Describe the morphology of the red blood cells.
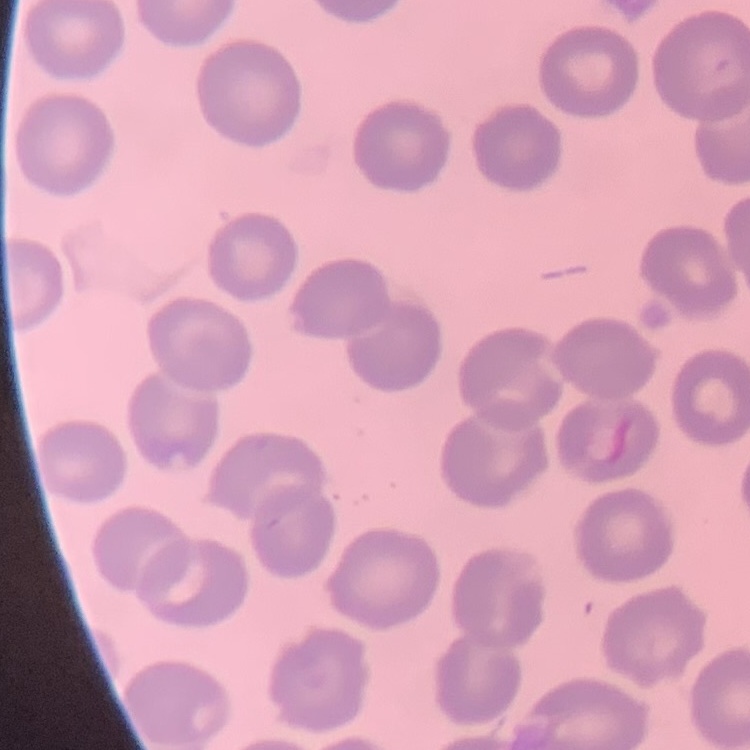
No rouleaux formation.

One tile cut from a larger photomicrograph. Thin blood smear. Field's or Giemsa stain.